Identify the parasite.
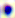
Toxoplasma gondii.

magnification = 400x
modality = photomicrograph